Assess this cell for malaria.
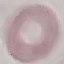

It is uninfected.

Summary:
  - Preparation: thin blood film
  - Image type: cell patch, automatically extracted from a larger field of view and resized to 64 × 64 pixels
  - Stain: Giemsa
  - Capture: smartphone through the microscope eyepiece